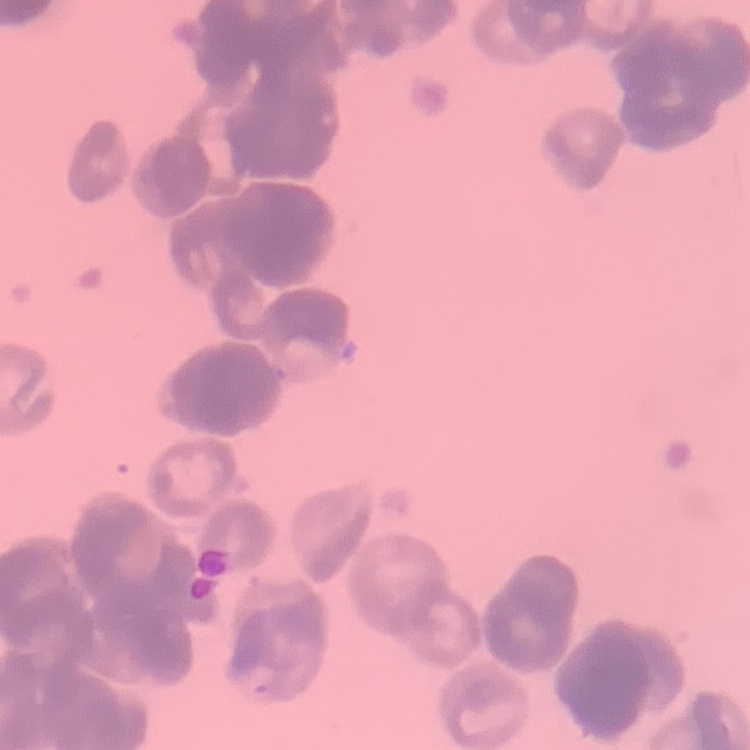

erythrocyte morphology = rouleaux formation
preparation = thin blood film
stain = Field's or Giemsa
image type = square crop of a larger photomicrograph